Report the malaria status of this cell.
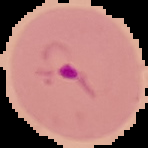
Parasitized.

The area outside the segmented cell region is set to black. Image is 148×148 pixels. From a thin blood film.